Identify the cell.
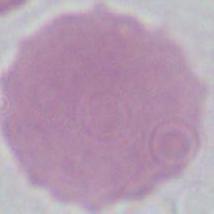
This is an erythrocyte.

Summary:
  - Modality: photomicrograph
  - Magnification: 1000x